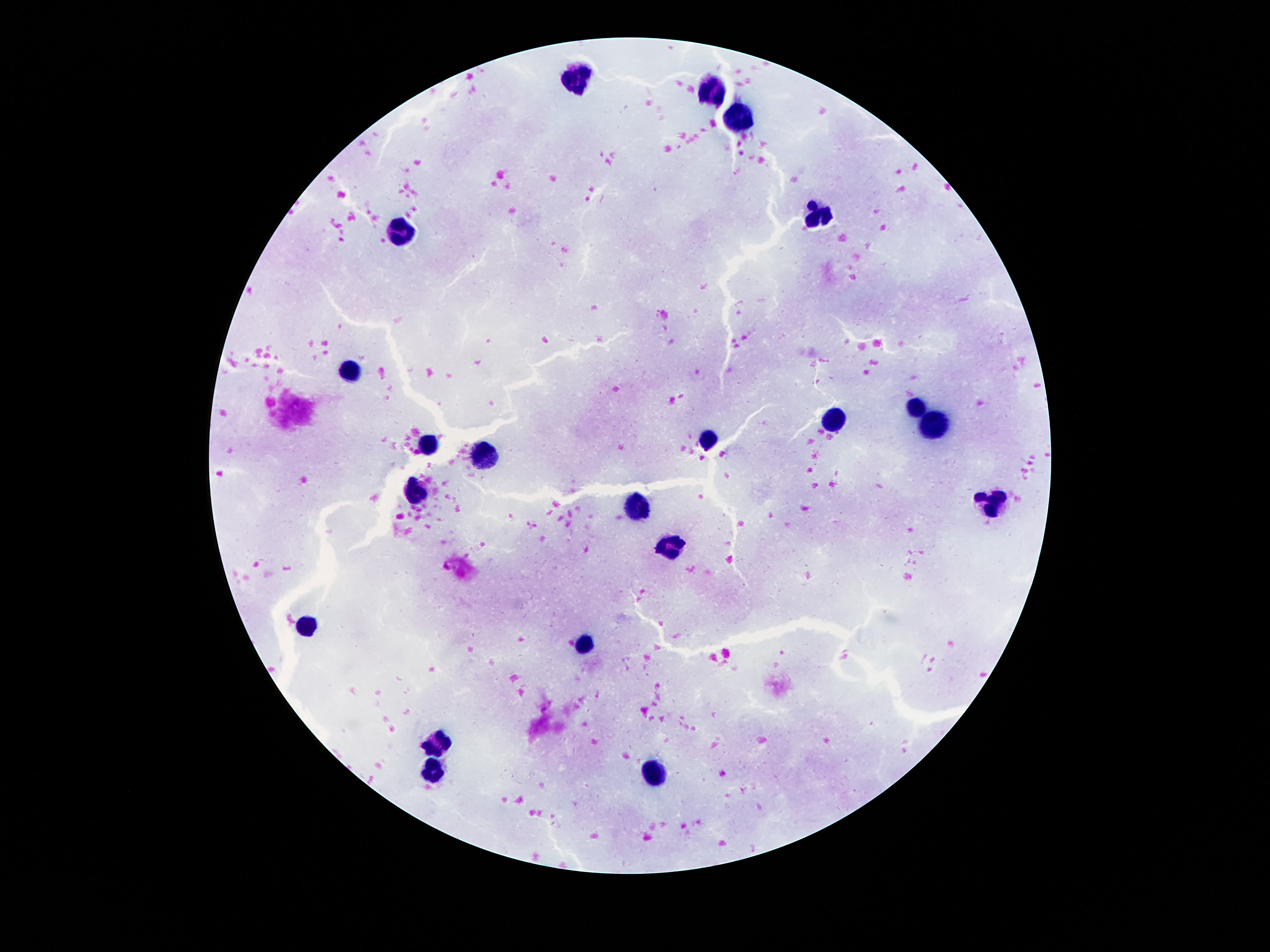

capture: smartphone camera through the microscope eyepiece
stain: Giemsa
patient_malaria_status: uninfected
image_size: 1270×952 pixels
preparation: thick blood smear
magnification: 100x
leukocyte_locations: 'approximate centers as [x, y] in pixels: [576, 77], [715, 90], [742, 117], [819, 216], [400, 229], [347, 370], [913, 405], [831, 419], [933, 421], [710, 442], [431, 444], [481, 453], [418, 494], [994, 503], [638, 504], [672, 544], [306, 628], [586, 644], [440, 744], [431, 771], [656, 772]'
field_of_view: single